Report the malaria status of this cell.
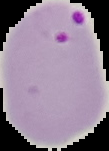

It is parasitized.

Summary:
  - Preparation: thin blood film
  - Image type: segmented cell region with the area outside set to black
  - Image size: 109×151 pixels